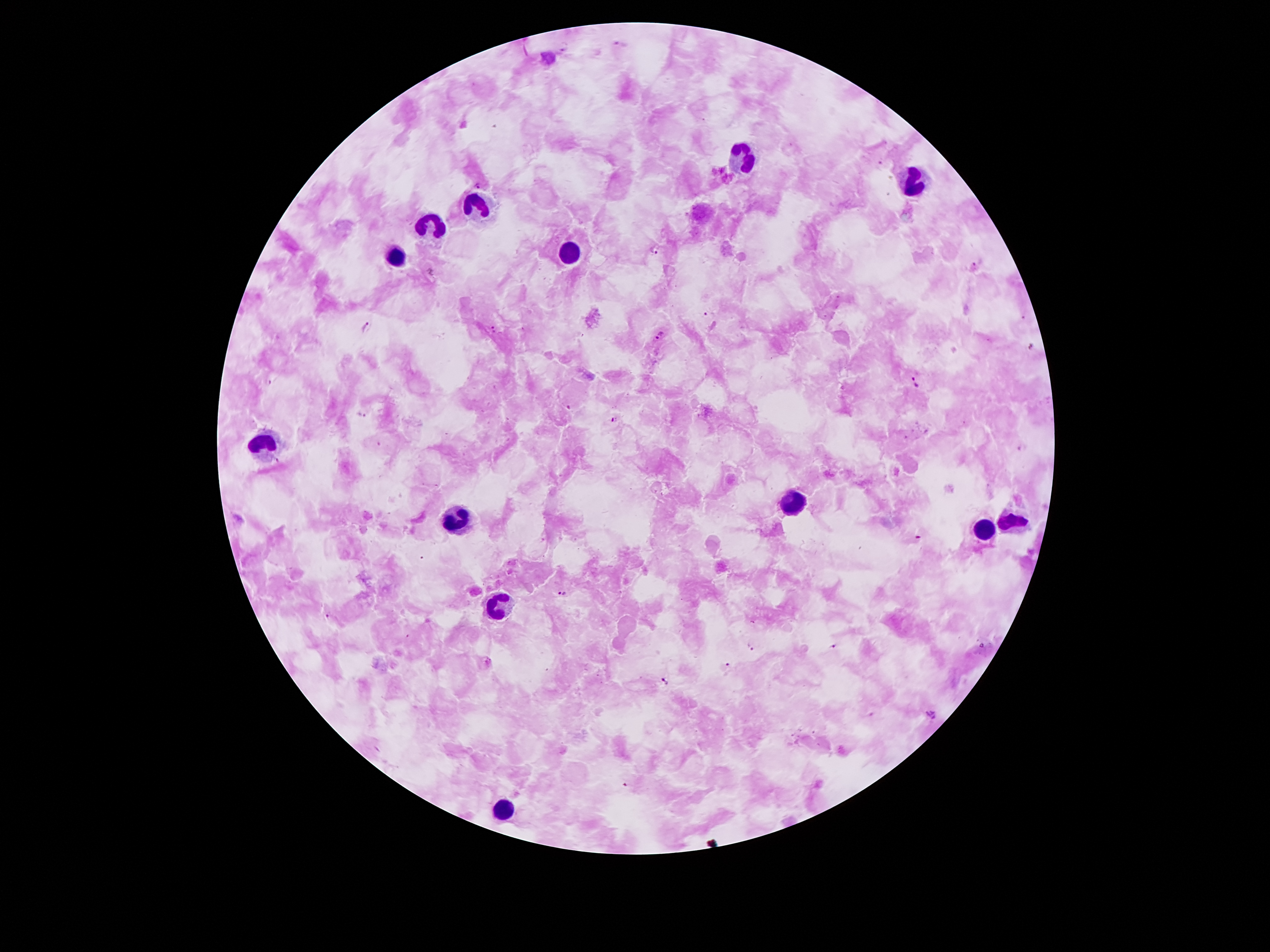

Approximate object centers, in pixels from the top-left corner.
Summary:
  - Leukocyte locations: (x=747, y=162), (x=912, y=182), (x=481, y=203), (x=429, y=220), (x=394, y=249), (x=568, y=249), (x=261, y=442), (x=793, y=504), (x=456, y=518), (x=1012, y=520), (x=985, y=529), (x=500, y=606), (x=505, y=805)
  - Plasmodium parasite locations: (x=881, y=163), (x=477, y=185), (x=655, y=251), (x=974, y=266), (x=707, y=314), (x=1024, y=317), (x=365, y=325), (x=493, y=329), (x=660, y=335), (x=1032, y=347), (x=269, y=382), (x=916, y=382), (x=567, y=406), (x=360, y=414), (x=614, y=419), (x=919, y=537), (x=562, y=593), (x=327, y=616), (x=752, y=647), (x=832, y=648), (x=729, y=664), (x=667, y=681), (x=932, y=714), (x=626, y=786)
  - Patient malaria status: positive for Plasmodium falciparum
  - Image size: 1270×952 pixels
  - Preparation: thick peripheral-blood smear
  - Stain: Giemsa
  - Magnification: 100x
  - Capture: smartphone through the microscope eyepiece
  - Field of view: one from this slide